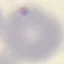 Malaria status: uninfected. Acquired by smartphone through the microscope eyepiece. Automatically extracted cell patch, resized to 64 × 64 pixels. Giemsa stain. Thin blood film.